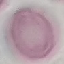
Summary:
  - Malaria status: uninfected
  - Image type: cell patch, automatically extracted from a larger field of view and resized to 64 × 64 pixels
  - Capture: smartphone through the microscope eyepiece
  - Preparation: thin smear
  - Stain: Giemsa